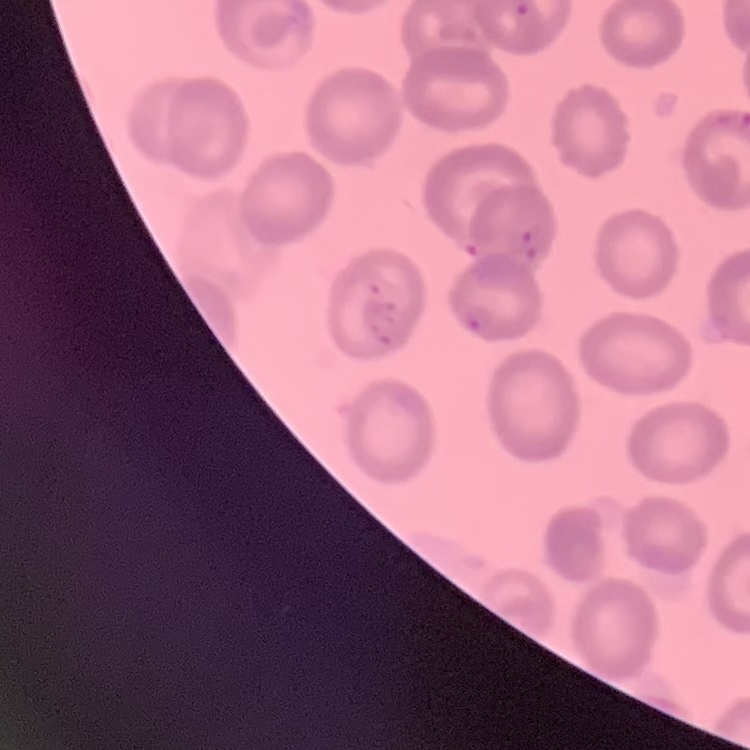
Summary:
  - Erythrocyte morphology: no rouleaux formation
  - Image type: one tile cut from a larger photomicrograph
  - Stain: Field's or Giemsa
  - Preparation: thin blood film